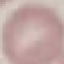

Malaria status: uninfected. Photographed with a smartphone camera at the microscope eyepiece. Automatically extracted cell patch, resized to 64 × 64 pixels. Giemsa stain. Thin blood smear.